State which parasite is depicted.
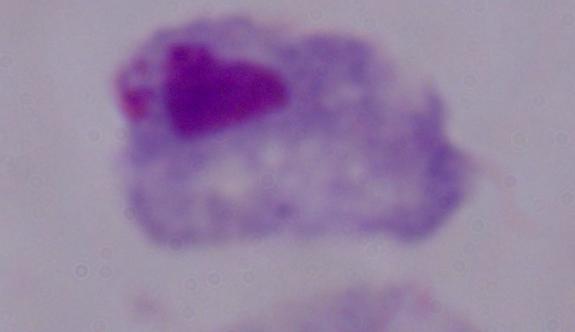

This is a trichomonad.

Photomicrograph. Captured at 1000x magnification.